Outline each blood parasite and name the species.
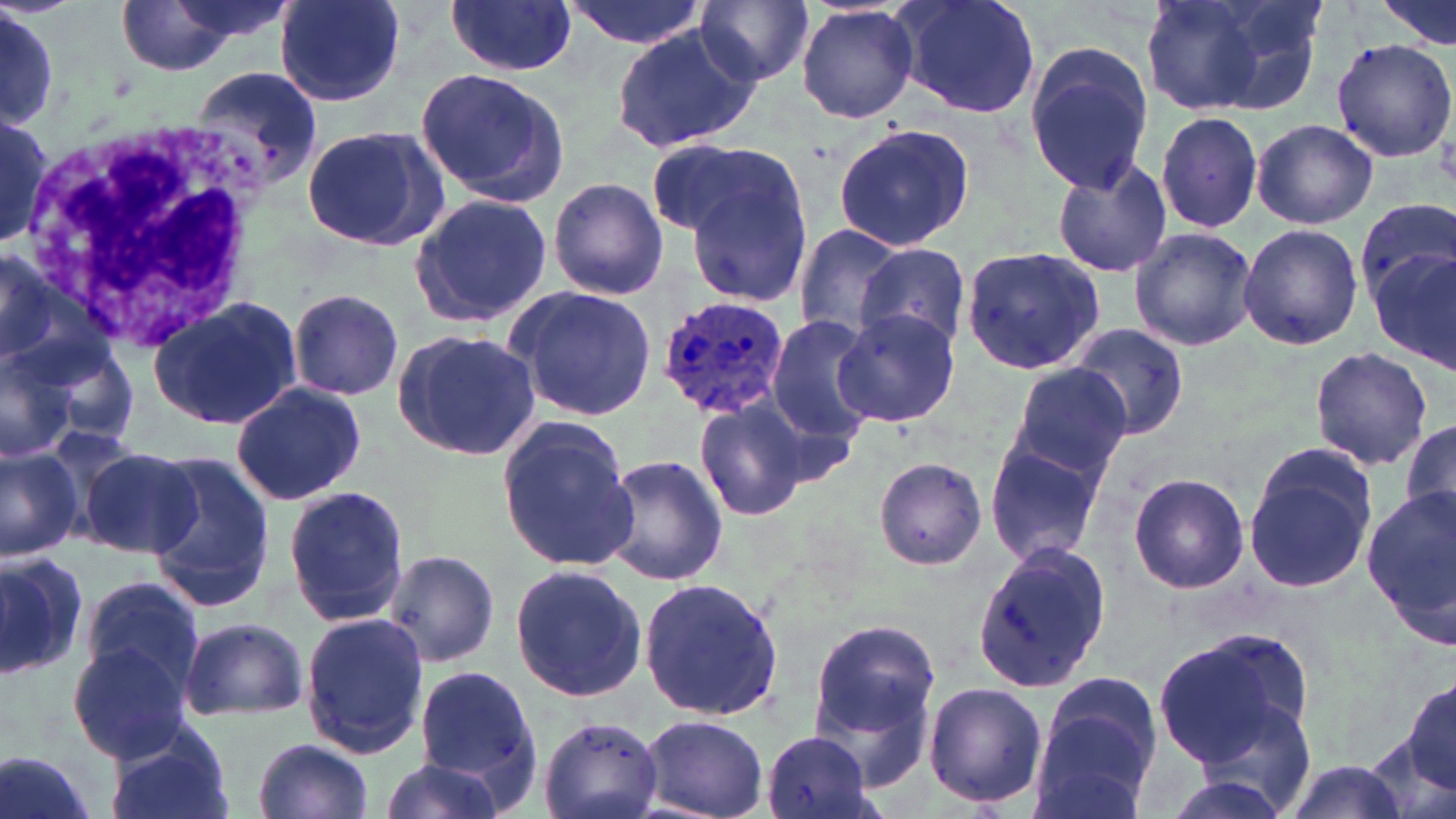

Approximate bounding boxes as (x1, y1, x2, y2) in pixels.
Plasmodium ovale-infected red blood cells: (654, 294, 792, 421).
No Plasmodium falciparum, Plasmodium malariae, Plasmodium vivax, Babesia divergens, or Trypanosoma brucei observed.

White blood cell locations: (21, 118, 265, 352). Uninfected red blood cell locations: (113, 0, 248, 77), (275, 0, 406, 105), (561, 0, 709, 48), (892, 0, 1044, 119), (1142, 0, 1325, 118), (1379, 0, 1454, 48), (445, 1, 577, 77), (696, 1, 814, 87), (1, 4, 58, 134), (796, 4, 920, 124), (609, 22, 764, 158), (1329, 38, 1456, 163), (1022, 39, 1156, 194), (189, 65, 325, 194), (416, 67, 568, 207), (1154, 109, 1265, 235), (0, 115, 54, 251), (0, 117, 55, 247), (1251, 118, 1379, 230), (301, 123, 453, 253), (831, 123, 975, 250), (645, 137, 796, 243), (667, 148, 816, 306), (1052, 155, 1174, 278), (548, 176, 669, 300), (408, 192, 555, 328), (1356, 198, 1456, 306), (1238, 222, 1363, 352), (791, 224, 911, 344), (1128, 226, 1256, 353), (856, 243, 971, 350), (0, 244, 88, 378), (1371, 247, 1456, 373), (961, 248, 1104, 372), (507, 283, 658, 422), (287, 288, 404, 401), (148, 297, 303, 430), (831, 307, 959, 427), (765, 318, 880, 443), (1059, 323, 1191, 442), (393, 328, 542, 462), (35, 334, 143, 449), (0, 345, 77, 462), (1310, 347, 1433, 470), (1003, 365, 1134, 486), (228, 383, 366, 505), (694, 399, 810, 522), (1401, 417, 1456, 530), (497, 419, 639, 573), (983, 439, 1108, 565), (0, 444, 82, 561), (75, 444, 199, 559), (1242, 444, 1380, 594), (144, 456, 273, 609), (599, 456, 728, 586), (873, 457, 987, 570), (1128, 472, 1248, 595), (282, 485, 410, 627), (1363, 490, 1456, 649), (970, 542, 1112, 696), (383, 548, 500, 668), (0, 549, 96, 676), (508, 563, 649, 701), (639, 576, 784, 725), (77, 577, 206, 702), (300, 611, 431, 759), (807, 617, 941, 755), (180, 618, 308, 721), (1152, 630, 1309, 770), (68, 643, 193, 764), (414, 664, 540, 795), (1032, 673, 1162, 814), (1403, 677, 1456, 794), (922, 681, 1048, 812), (638, 714, 770, 817), (537, 716, 664, 819), (106, 718, 233, 819), (761, 729, 880, 819), (252, 737, 375, 818), (0, 749, 103, 819), (1272, 755, 1413, 819), (374, 756, 511, 819). Slide-level diagnosis: Plasmodium ovale. Thin blood film. May-Grünwald-Giemsa stain. Image is 1456×819 pixels. Light microscopy. Single field of view. Captured at 1000x magnification.